Classify this cell by malaria status.
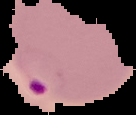

It is parasitized.

Image is 136×115 pixels. The area outside the segmented cell region is set to black. From a thin blood film.